Identify the blood parasite species.
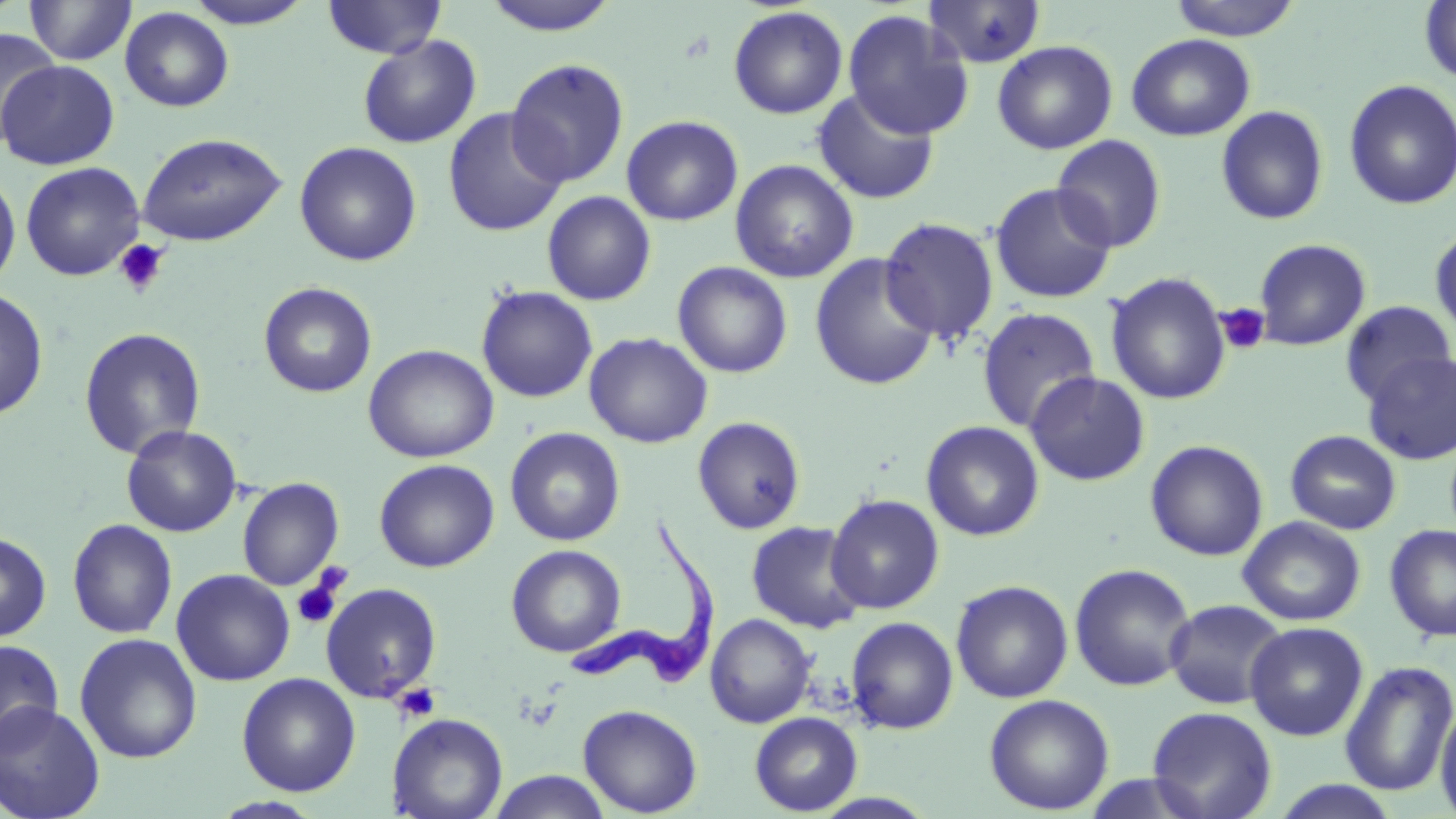

Trypanosoma brucei.

Summary:
  - Coordinate format: approximate bounding boxes as (x1, y1, x2, y2) in pixels
  - Platelet locations: (114, 239, 169, 297), (1215, 303, 1271, 355), (291, 572, 345, 629), (393, 681, 442, 723)
  - Uninfected red blood cell locations: (323, 0, 446, 59), (480, 0, 621, 36), (1166, 0, 1304, 40), (26, 1, 137, 66), (183, 1, 315, 29), (924, 1, 1047, 69), (1419, 1, 1455, 85), (119, 6, 234, 112), (727, 6, 849, 119), (842, 9, 975, 140), (1, 26, 61, 143), (1126, 33, 1256, 141), (357, 34, 482, 149), (992, 40, 1118, 154), (505, 57, 630, 188), (1, 61, 119, 170), (1343, 79, 1456, 210), (812, 88, 940, 205), (1216, 105, 1329, 225), (442, 107, 568, 238), (621, 115, 743, 226), (138, 132, 287, 247), (1051, 134, 1167, 252), (294, 141, 422, 266), (730, 159, 859, 283), (20, 161, 145, 281), (0, 169, 21, 290), (990, 182, 1117, 304), (541, 191, 656, 305), (879, 217, 1000, 345), (1429, 224, 1456, 342), (1253, 238, 1371, 351), (809, 253, 939, 391), (672, 261, 793, 378), (1105, 271, 1231, 405), (258, 281, 377, 398), (476, 285, 598, 403), (0, 286, 49, 420), (1339, 300, 1455, 407), (976, 307, 1100, 432), (78, 327, 206, 460), (584, 332, 713, 448), (363, 344, 499, 463), (1361, 351, 1456, 465), (1025, 371, 1150, 486), (692, 416, 807, 535), (920, 420, 1044, 541), (121, 425, 242, 536), (504, 427, 626, 547), (1285, 430, 1402, 535), (1145, 440, 1268, 561), (374, 458, 499, 573), (237, 477, 344, 590), (826, 494, 944, 614), (1238, 516, 1366, 627), (67, 519, 178, 639), (746, 520, 867, 633), (1383, 523, 1456, 642), (0, 531, 51, 642), (506, 544, 626, 657), (1069, 562, 1196, 691), (171, 569, 295, 686), (950, 580, 1074, 704), (320, 582, 442, 704), (1164, 599, 1288, 709), (705, 613, 816, 728), (845, 616, 959, 734), (1245, 622, 1368, 741), (75, 633, 202, 764), (0, 639, 64, 753), (1340, 659, 1456, 796), (236, 672, 361, 797), (984, 694, 1114, 815), (0, 700, 106, 819), (1435, 702, 1456, 819), (578, 703, 703, 817), (1147, 706, 1278, 819), (749, 712, 863, 815), (388, 713, 508, 819), (487, 770, 613, 819), (1268, 778, 1405, 819), (208, 796, 326, 818)
  - Trypanosoma brucei locations: (565, 523, 721, 694)
  - Preparation: thin blood film
  - Image size: 1456×819 pixels
  - Magnification: 1000x
  - Modality: light microscopy
  - Stain: May-Grünwald-Giemsa
  - Field of view: one of a larger specimen